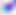
{
  "magnification": "400x",
  "modality": "micrograph",
  "identification": "Toxoplasma gondii"
}